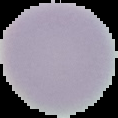 Result: no malaria parasites detected. Cell region segmented out of the field of view; the surrounding area is masked to black. Image is 118×118 pixels. From a thin blood smear.